Name the parasite shown.
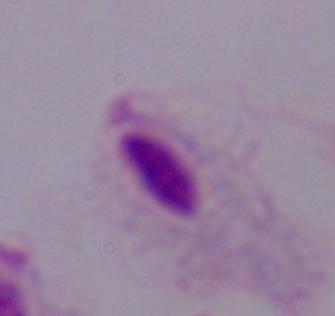
This is a trichomonad.

modality = photomicrograph
magnification = 1000x